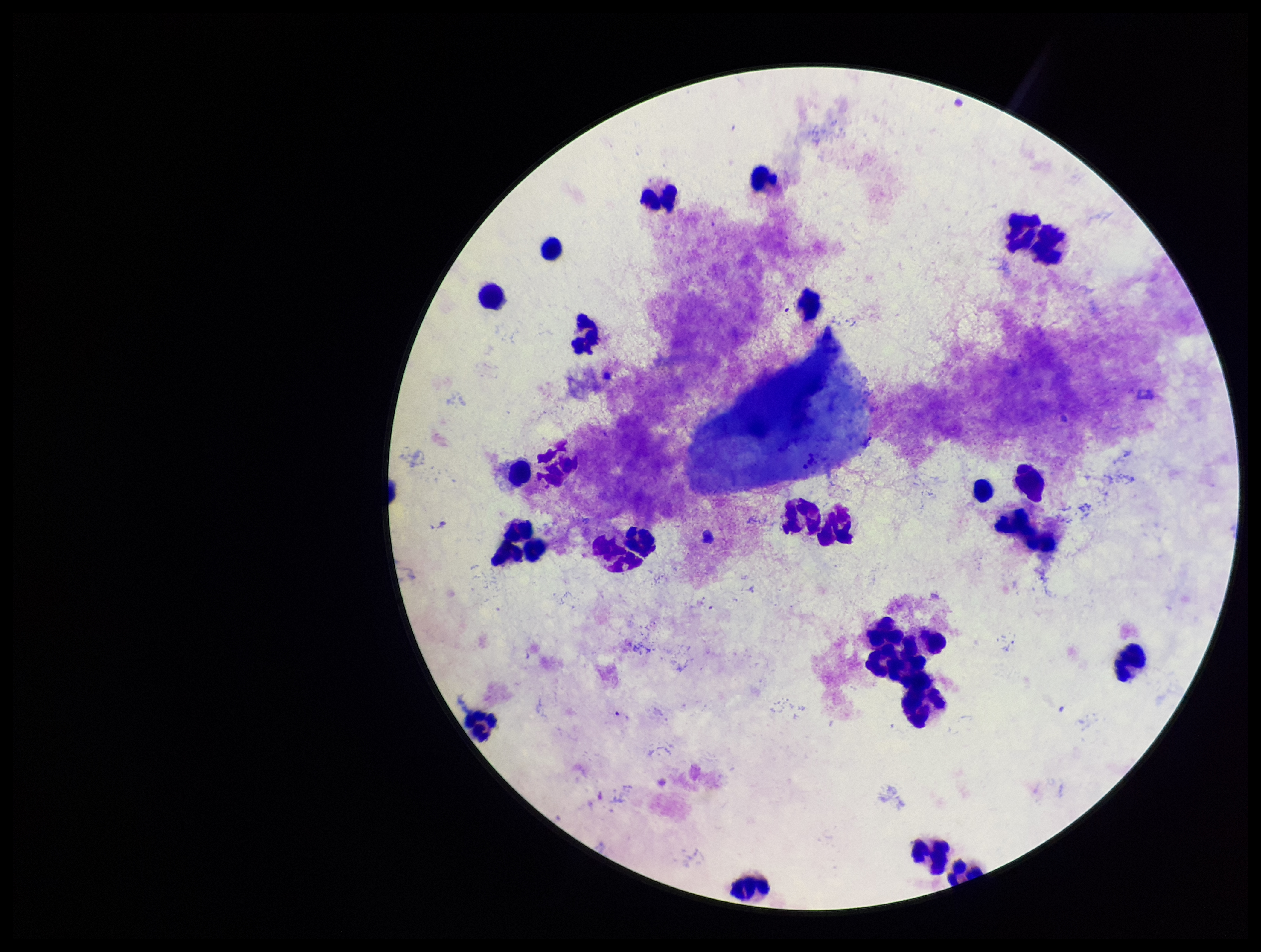
Preparation: thick smear. Plasmodium parasites: none identified. Stained with Giemsa. Leukocyte count: 27. Image is 1261×952 pixels. Parasite count: 0. Smartphone photograph taken through the eyepiece of a microscope. Patient malaria status: negative. One field from this slide.